Identify the blood parasite species.
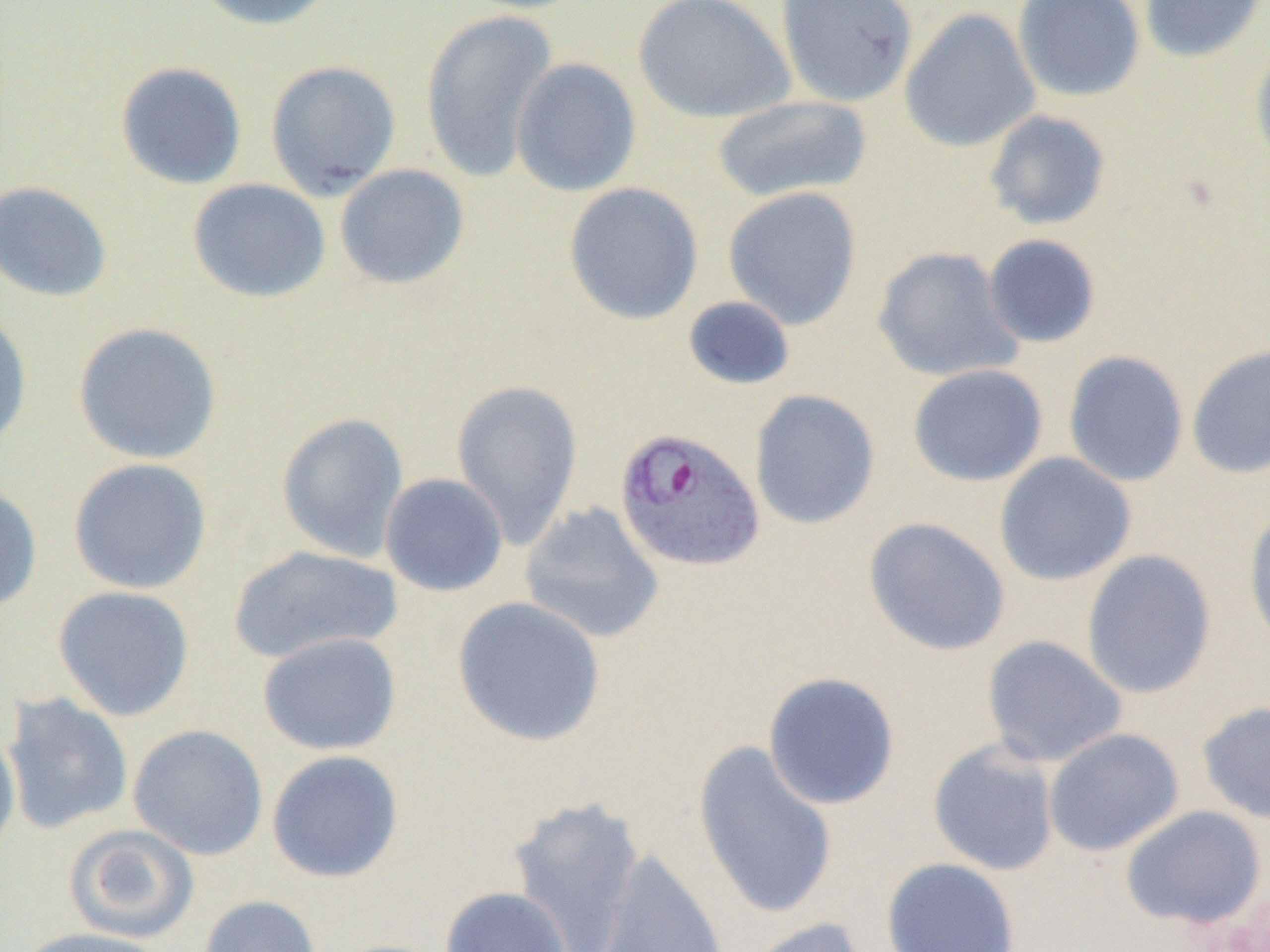
Plasmodium ovale.

Summary:
  - Coordinate format: approximate bounding boxes as (x1,y1)-(x2,y2) corner pairs in pixels
  - Plasmodium ovale-infected red blood cell locations: (613,426)-(766,573)
  - Uninfected red blood cell locations: (192,0)-(339,32), (456,0)-(595,14), (633,0)-(795,124), (775,0)-(918,108), (1012,0)-(1146,103), (1139,0)-(1267,63), (899,7)-(1041,153), (420,10)-(559,183), (1250,45)-(1270,173), (510,57)-(641,197), (265,60)-(401,199), (115,61)-(247,190), (712,95)-(873,204), (983,109)-(1112,231), (334,163)-(470,289), (187,178)-(331,303), (0,180)-(113,303), (563,182)-(704,326), (723,186)-(863,330), (982,233)-(1102,349), (872,246)-(1023,383), (682,295)-(796,391), (0,309)-(33,454), (73,321)-(223,464), (1187,343)-(1270,480), (1062,350)-(1189,487), (908,364)-(1048,486), (450,377)-(584,549), (749,389)-(881,531), (276,412)-(410,562), (994,452)-(1137,586), (67,457)-(213,595), (380,473)-(509,597), (0,485)-(43,614), (520,501)-(665,644), (1243,508)-(1270,651), (863,517)-(1011,656), (227,545)-(403,665), (1081,549)-(1217,699), (52,585)-(195,721), (452,595)-(607,747), (257,631)-(402,755), (981,635)-(1127,768), (762,671)-(901,810), (2,692)-(135,834), (1197,701)-(1270,825), (0,719)-(20,857), (128,723)-(269,860), (1043,728)-(1184,856), (692,739)-(838,922), (927,739)-(1060,877), (266,749)-(404,883), (507,795)-(646,952), (1120,805)-(1267,930), (64,824)-(200,943), (592,849)-(729,952), (881,857)-(1021,952), (439,886)-(573,952), (198,894)-(322,952), (745,916)-(873,952), (16,927)-(170,952)
  - Field of view: one of a larger specimen
  - Magnification: 1000x
  - Modality: optical microscopy
  - Image size: 1270×952 pixels
  - Preparation: thin blood film